Assess the morphology of the red blood cells.
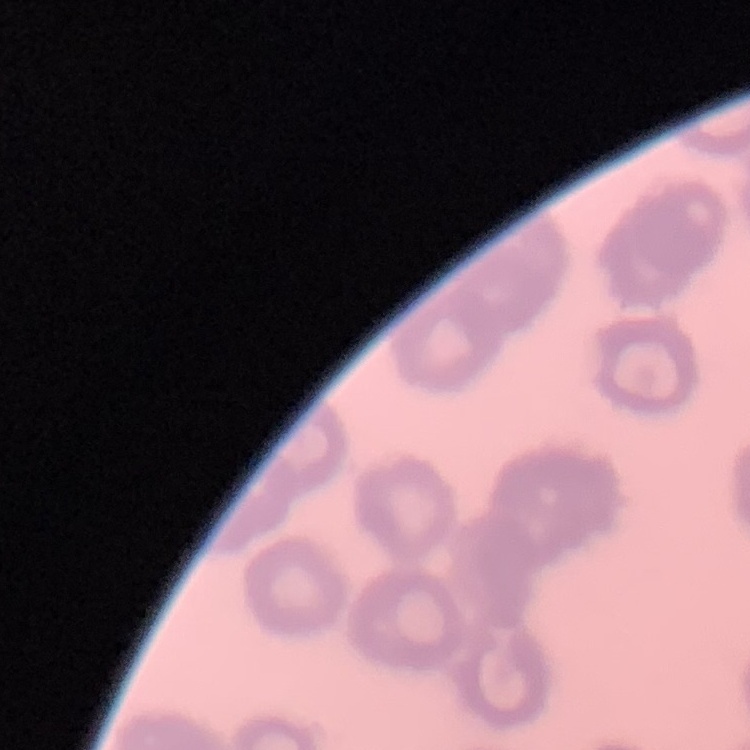

They show rouleaux formation.

preparation = thin peripheral smear
image type = square crop of a larger photomicrograph
stain = Field's or Giemsa